State which parasite is depicted.
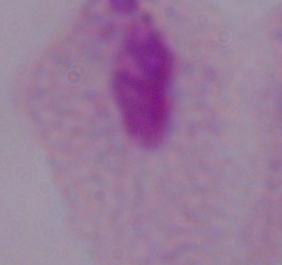

A trichomonad.

Micrograph. 1000x magnification.